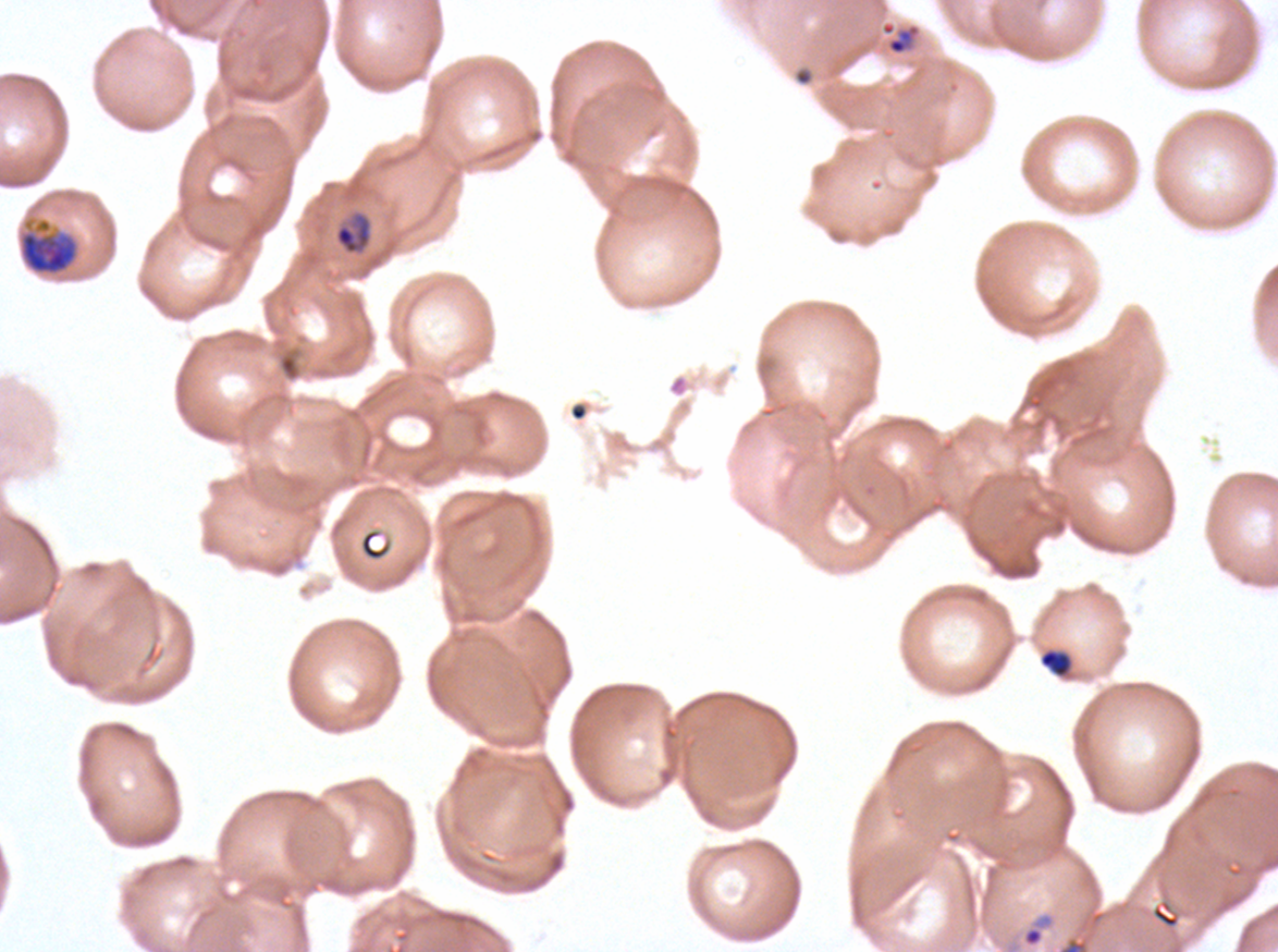
Approximate bounding boxes as [x1, y1, x2, y2] in pixels. Ring locations: [1021, 912, 1053, 948]. Late trophozoite locations: [18, 216, 80, 276]. Late-ring/early-trophozoite locations: [886, 23, 921, 56], [334, 211, 373, 255], [1038, 649, 1072, 677]. Image is 1278×952 pixels. One sub-image of a larger composite. P. falciparum from a patient in The Gambia, cultured ex vivo for 24 to 48 hours. Giemsa stain. Life-cycle stages observed: ring, late-ring/early-trophozoite, late trophozoite. Thin blood smear.